Assess this cell for malaria.
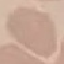
Uninfected.

Summary:
  - Stain: Giemsa
  - Image type: automatically extracted cell patch, resized to 64 × 64 pixels
  - Preparation: thin smear
  - Capture: smartphone camera at the microscope eyepiece